Locate every uninfected red blood cell.
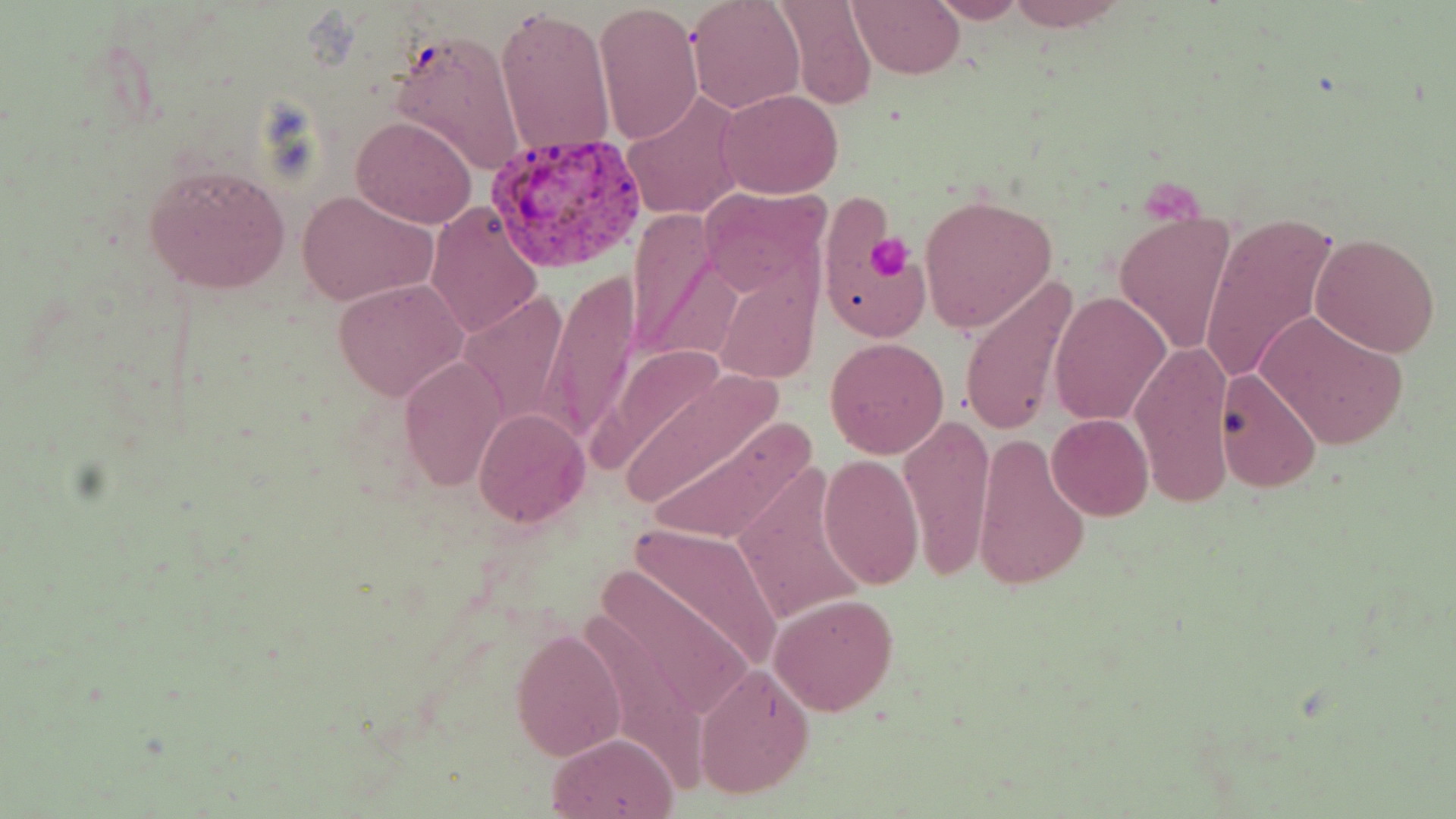
Approximate bounding boxes as [x1, y1, x2, y2] in pixels.
Uninfected red blood cells: [687, 0, 807, 114], [772, 0, 878, 111], [847, 0, 964, 77], [928, 0, 1028, 24], [1005, 0, 1132, 30], [594, 2, 704, 144], [495, 6, 616, 160], [389, 29, 524, 175], [718, 89, 841, 199], [621, 92, 743, 220], [350, 114, 477, 228], [143, 160, 291, 294], [697, 184, 831, 301], [295, 189, 438, 307], [918, 194, 1058, 333], [426, 202, 542, 338], [627, 209, 728, 364], [1113, 211, 1236, 357], [1198, 211, 1342, 386], [1311, 233, 1441, 357], [958, 271, 1080, 437], [716, 274, 819, 386], [541, 275, 642, 442], [333, 278, 468, 402], [458, 291, 572, 429], [1049, 292, 1171, 428], [1257, 309, 1408, 451], [825, 337, 948, 459], [1130, 338, 1235, 507], [400, 353, 506, 491], [612, 361, 779, 514], [1215, 367, 1326, 496], [474, 408, 589, 528], [899, 410, 998, 582], [639, 413, 813, 550], [1047, 414, 1152, 521], [970, 431, 1090, 592], [817, 453, 923, 590], [731, 468, 872, 630], [625, 521, 785, 673], [593, 562, 760, 729], [770, 593, 897, 716], [512, 628, 626, 760], [694, 663, 816, 800], [547, 733, 680, 819].

Plasmodium vivax-infected red blood cell locations: [486, 133, 649, 272]. Platelet locations: [1142, 183, 1204, 229], [863, 233, 912, 281]. Slide-level diagnosis: Plasmodium vivax. Image is 1456×819 pixels. Captured at 1000x magnification. Optical microscopy. Thin blood smear. May-Grünwald-Giemsa-stained preparation. One field of a larger specimen.